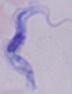
Summary:
  - Magnification: 1000x
  - Identification: trypanosome
  - Modality: photomicrograph